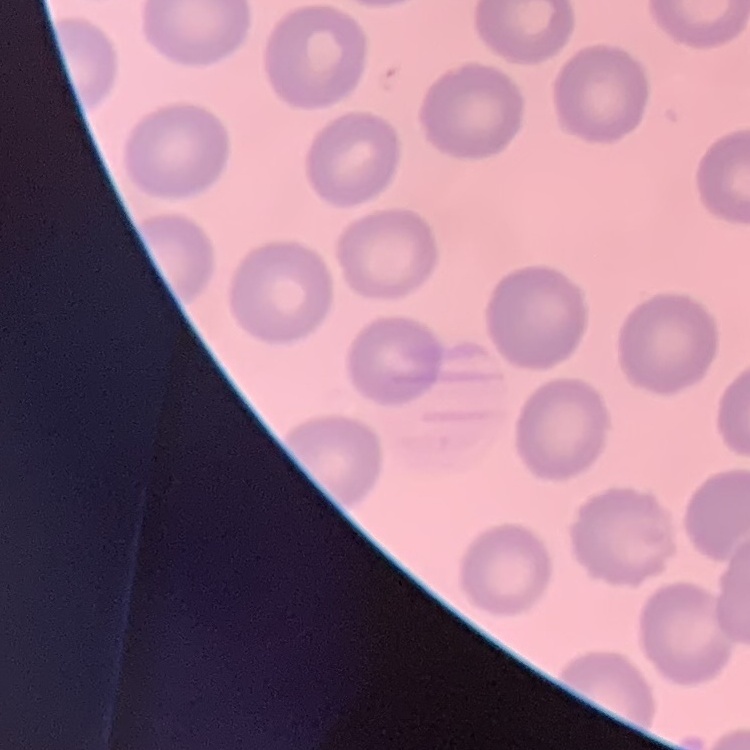

red blood cell morphology = no rouleaux formation
preparation = thin blood film
stain = Field's or Giemsa
image type = square crop of a larger photomicrograph